Identify the cell.
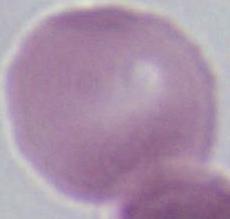
An erythrocyte.

modality = photomicrograph
magnification = 1000x